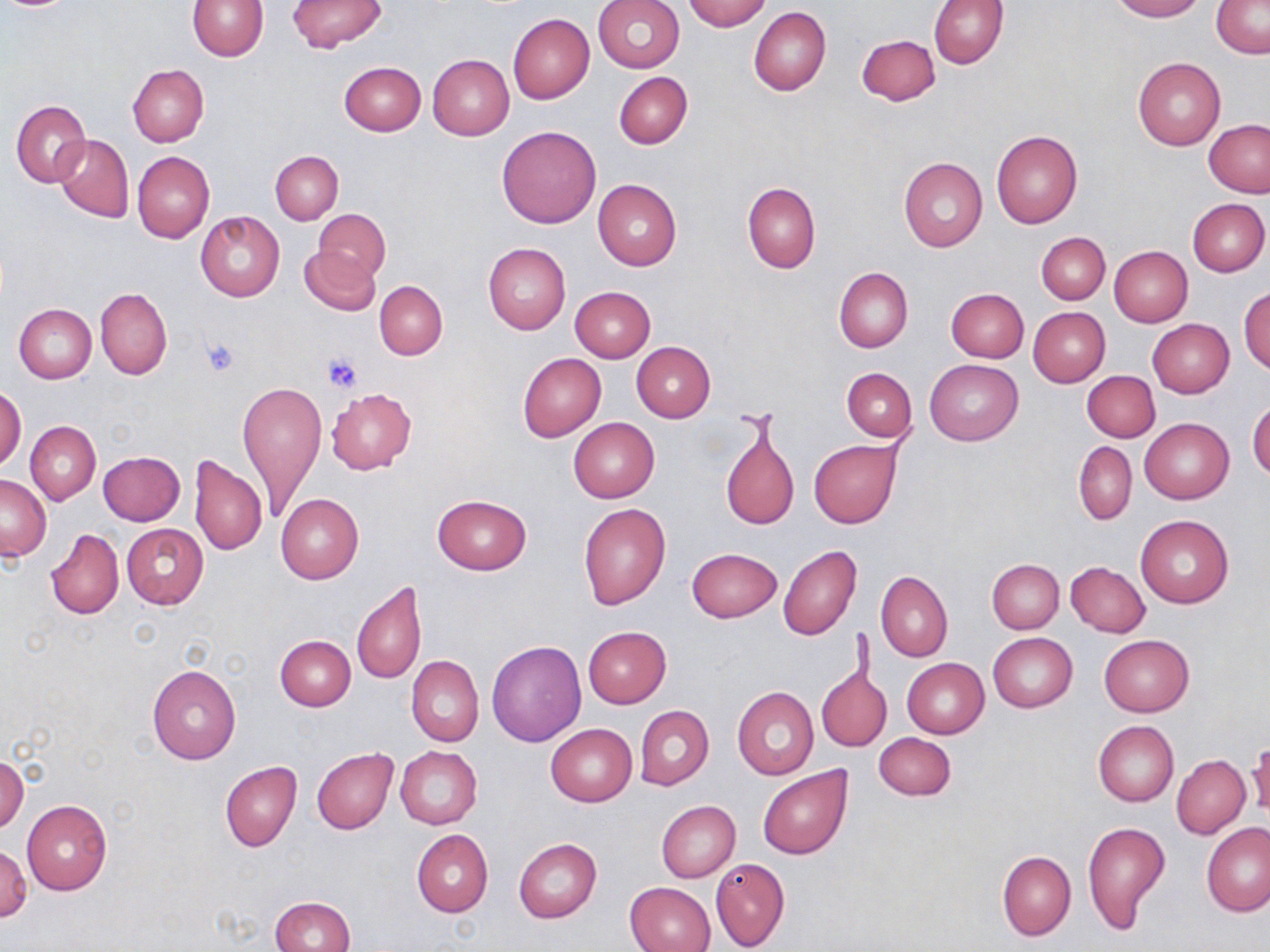
Summary:
  - Coordinate format: approximate bounding boxes as named x1/y1/x2/y2 corners in pixels
  - Uninfected red blood cell locations: (x1=186, y1=0, x2=268, y2=60), (x1=594, y1=0, x2=685, y2=73), (x1=684, y1=0, x2=770, y2=31), (x1=929, y1=0, x2=1009, y2=69), (x1=1111, y1=0, x2=1204, y2=21), (x1=287, y1=1, x2=387, y2=52), (x1=1211, y1=1, x2=1270, y2=57), (x1=749, y1=7, x2=830, y2=96), (x1=508, y1=14, x2=594, y2=104), (x1=856, y1=34, x2=941, y2=106), (x1=427, y1=54, x2=514, y2=140), (x1=1132, y1=57, x2=1224, y2=151), (x1=339, y1=61, x2=425, y2=135), (x1=127, y1=64, x2=209, y2=146), (x1=615, y1=72, x2=693, y2=148), (x1=11, y1=100, x2=90, y2=186), (x1=1204, y1=120, x2=1270, y2=197), (x1=496, y1=125, x2=601, y2=228), (x1=991, y1=130, x2=1082, y2=228), (x1=53, y1=133, x2=133, y2=223), (x1=270, y1=150, x2=343, y2=224), (x1=132, y1=151, x2=214, y2=243), (x1=899, y1=158, x2=987, y2=253), (x1=593, y1=179, x2=681, y2=271), (x1=742, y1=181, x2=820, y2=273), (x1=1187, y1=197, x2=1268, y2=276), (x1=314, y1=210, x2=390, y2=281), (x1=196, y1=211, x2=285, y2=301), (x1=1037, y1=232, x2=1110, y2=305), (x1=483, y1=243, x2=570, y2=333), (x1=299, y1=246, x2=380, y2=315), (x1=1109, y1=246, x2=1192, y2=327), (x1=834, y1=268, x2=913, y2=353), (x1=374, y1=281, x2=447, y2=360), (x1=570, y1=286, x2=655, y2=361), (x1=1239, y1=286, x2=1269, y2=373), (x1=96, y1=287, x2=172, y2=381), (x1=946, y1=288, x2=1029, y2=362), (x1=13, y1=303, x2=97, y2=383), (x1=1028, y1=307, x2=1110, y2=387), (x1=1147, y1=318, x2=1234, y2=397), (x1=631, y1=342, x2=714, y2=423), (x1=517, y1=352, x2=604, y2=440), (x1=926, y1=358, x2=1023, y2=445), (x1=841, y1=367, x2=916, y2=443), (x1=1082, y1=371, x2=1159, y2=442), (x1=238, y1=380, x2=326, y2=518), (x1=1, y1=386, x2=26, y2=470), (x1=326, y1=388, x2=416, y2=474), (x1=1247, y1=398, x2=1270, y2=481), (x1=568, y1=418, x2=660, y2=503), (x1=1140, y1=418, x2=1234, y2=504), (x1=25, y1=421, x2=100, y2=505), (x1=719, y1=422, x2=798, y2=531), (x1=809, y1=440, x2=901, y2=529), (x1=1074, y1=441, x2=1136, y2=524), (x1=106, y1=450, x2=190, y2=602), (x1=98, y1=451, x2=185, y2=526), (x1=190, y1=455, x2=267, y2=555), (x1=0, y1=473, x2=51, y2=559), (x1=276, y1=493, x2=364, y2=582), (x1=431, y1=494, x2=531, y2=574), (x1=578, y1=502, x2=671, y2=610), (x1=1136, y1=514, x2=1233, y2=607), (x1=121, y1=524, x2=208, y2=609), (x1=47, y1=528, x2=123, y2=620), (x1=778, y1=545, x2=861, y2=640), (x1=686, y1=547, x2=782, y2=623), (x1=987, y1=558, x2=1063, y2=633), (x1=1065, y1=562, x2=1149, y2=637), (x1=877, y1=572, x2=953, y2=662), (x1=352, y1=581, x2=424, y2=685), (x1=583, y1=626, x2=671, y2=707), (x1=988, y1=632, x2=1078, y2=712), (x1=274, y1=635, x2=355, y2=711), (x1=1099, y1=635, x2=1193, y2=717), (x1=486, y1=641, x2=586, y2=747), (x1=407, y1=655, x2=483, y2=747), (x1=902, y1=658, x2=989, y2=739), (x1=146, y1=664, x2=241, y2=764), (x1=817, y1=666, x2=889, y2=753), (x1=732, y1=686, x2=818, y2=779), (x1=635, y1=705, x2=714, y2=790), (x1=1093, y1=721, x2=1178, y2=807), (x1=546, y1=724, x2=637, y2=805), (x1=875, y1=732, x2=957, y2=801), (x1=1247, y1=742, x2=1270, y2=817), (x1=395, y1=746, x2=482, y2=829), (x1=312, y1=748, x2=398, y2=833), (x1=0, y1=754, x2=28, y2=833), (x1=1171, y1=755, x2=1250, y2=839), (x1=220, y1=761, x2=301, y2=852), (x1=756, y1=766, x2=853, y2=860), (x1=21, y1=800, x2=112, y2=894), (x1=656, y1=800, x2=741, y2=882), (x1=1082, y1=821, x2=1172, y2=936), (x1=1201, y1=822, x2=1270, y2=915), (x1=412, y1=830, x2=493, y2=918), (x1=513, y1=839, x2=602, y2=923), (x1=0, y1=842, x2=32, y2=923), (x1=997, y1=850, x2=1076, y2=941), (x1=710, y1=857, x2=790, y2=951), (x1=623, y1=882, x2=715, y2=951), (x1=270, y1=897, x2=355, y2=952)
  - Platelet locations: (x1=198, y1=337, x2=242, y2=377), (x1=321, y1=352, x2=364, y2=393)
  - Slide-level diagnosis: no evidence of blood parasites
  - Stain: May-Grünwald-Giemsa
  - Modality: optical microscopy
  - Image size: 1270×952 pixels
  - Field of view: one of a larger specimen
  - Preparation: thin blood film
  - Magnification: 1000x